Assess for malaria.
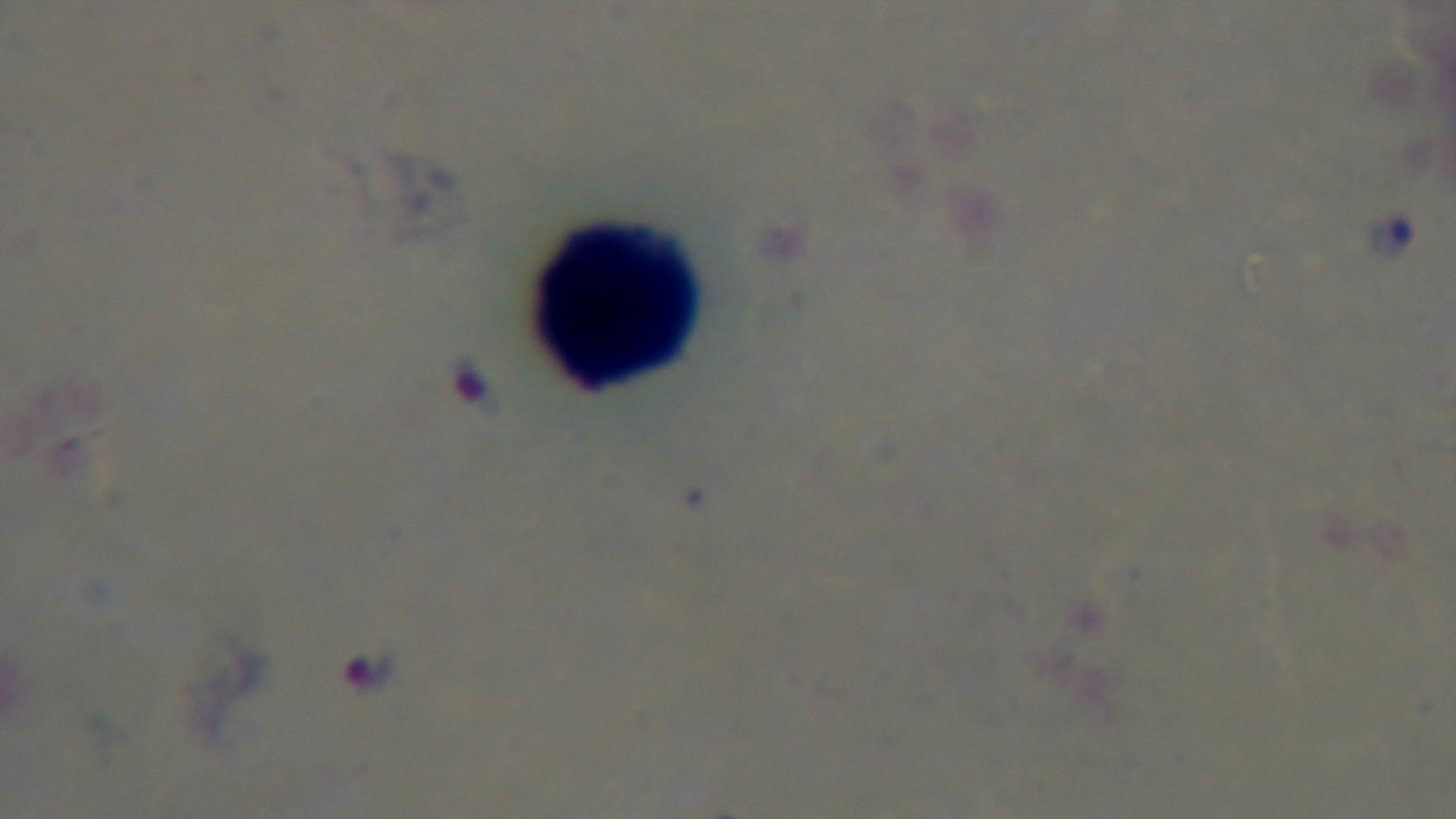

Infected.

Summary:
  - Preparation: thick smear
  - Field of view: single
  - Capture: mounted 4K digital camera
  - Modality: light microscopy
  - Stain: Giemsa
  - Objective: 100x oil immersion